Describe the morphology of the erythrocytes.
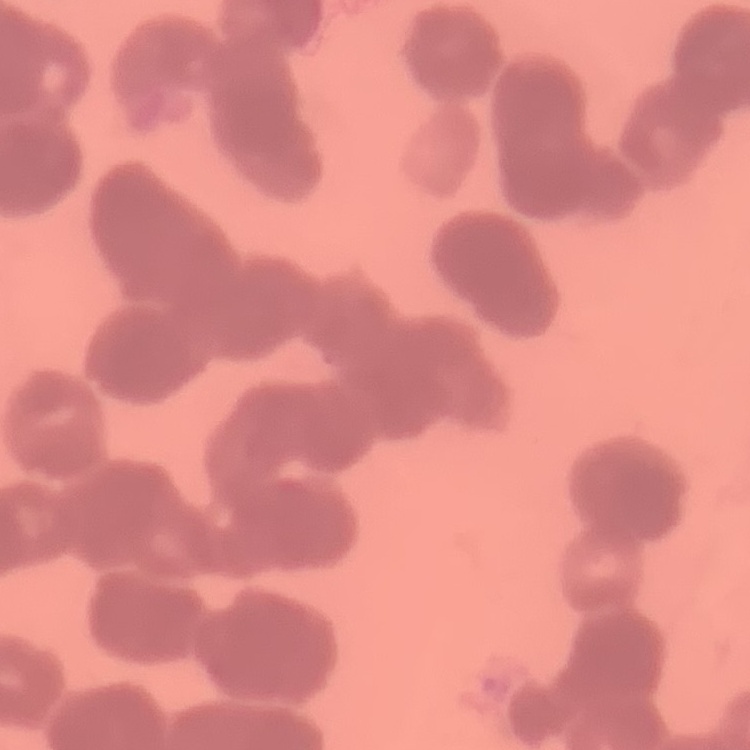
Rouleaux formation.

Summary:
  - Preparation: thin peripheral smear
  - Image type: square crop of a larger photomicrograph
  - Stain: Field's or Giemsa